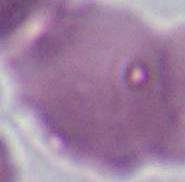 Photomicrograph. A red blood cell is shown. Captured at 1000x magnification.